Report the malaria status of this cell.
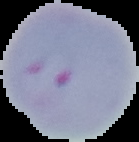
Parasitized.

Image is 139×142 pixels. From a thin blood smear. Segmented cell region on a black background.